Assess the morphology of the erythrocytes.
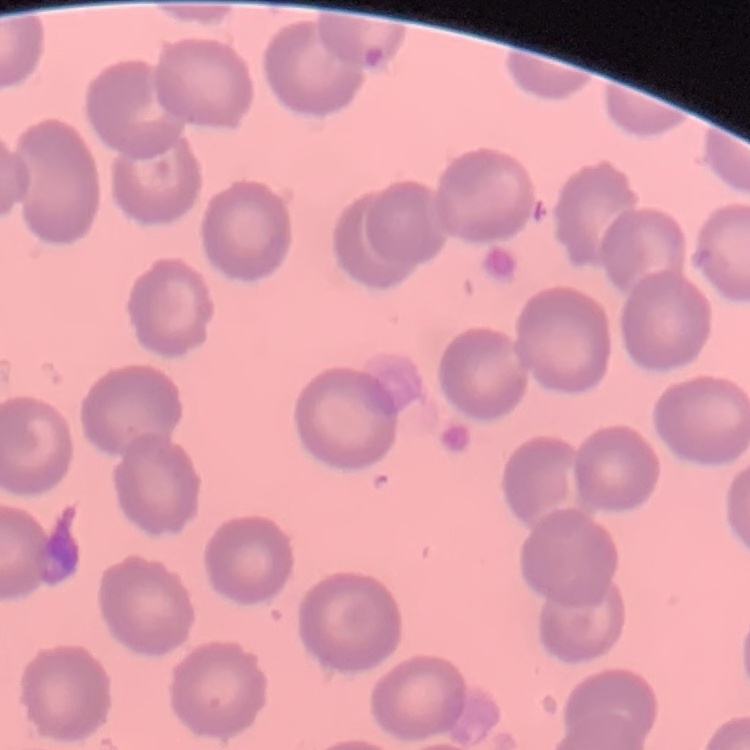

They show no rouleaux formation.

Summary:
  - Stain: Field's or Giemsa
  - Preparation: thin blood film
  - Image type: square crop of a larger photomicrograph